Point out each leukocyte.
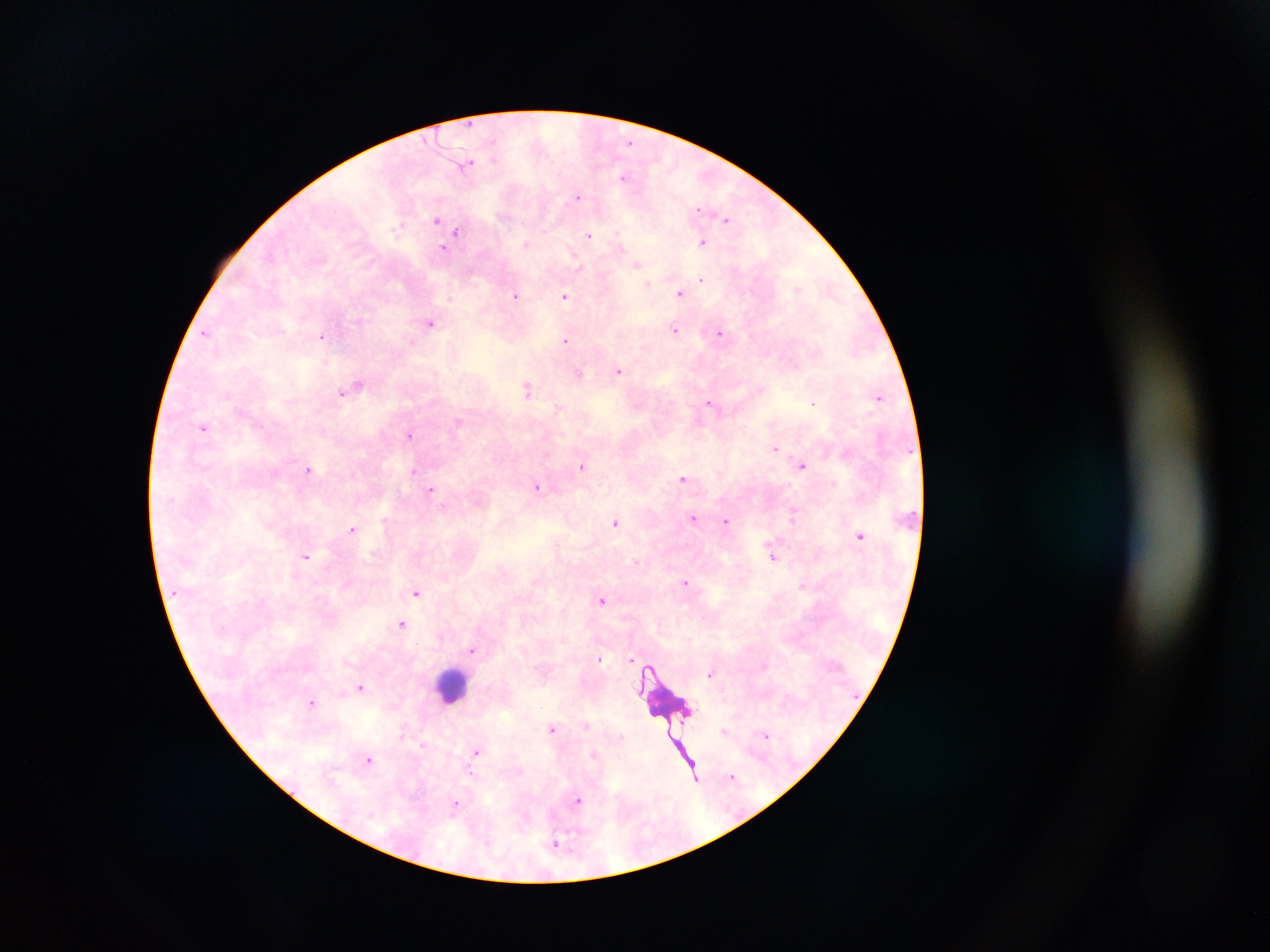

Approximate centers as x y in pixels.
Leukocytes: 451 685; 665 710.

Summary:
  - Plasmodium parasite locations: 629 142; 466 163; 624 176; 578 196; 698 209; 727 218; 437 219; 396 228; 457 233; 589 235; 454 237; 702 242; 525 244; 443 248; 637 264; 578 266; 701 279; 648 284; 797 289; 680 292; 516 294; 565 296; 430 322; 675 331; 205 332; 720 333; 321 336; 565 340; 619 371; 579 373; 359 385; 350 388; 526 389; 341 392; 879 397; 709 402; 813 403; 458 422; 203 428; 410 433; 776 448; 803 465; 582 466; 309 470; 414 471; 683 478; 537 487; 431 489; 443 506; 693 517; 793 517; 386 521; 726 521; 615 522; 352 529; 860 536; 772 556; 307 557; 635 560; 685 582; 802 586; 416 593; 602 600; 402 624; 472 650; 601 659; 630 660; 711 674; 361 687; 312 702; 586 725; 553 729; 723 731; 766 735; 476 751; 594 754; 368 759; 732 776; 694 777; 578 801; 455 806; 557 844
  - Country: Ghana
  - Image size: 1270×952 pixels
  - Preparation: thick blood film
  - Field of view: single
  - Capture: mobile-phone photograph through a microscope